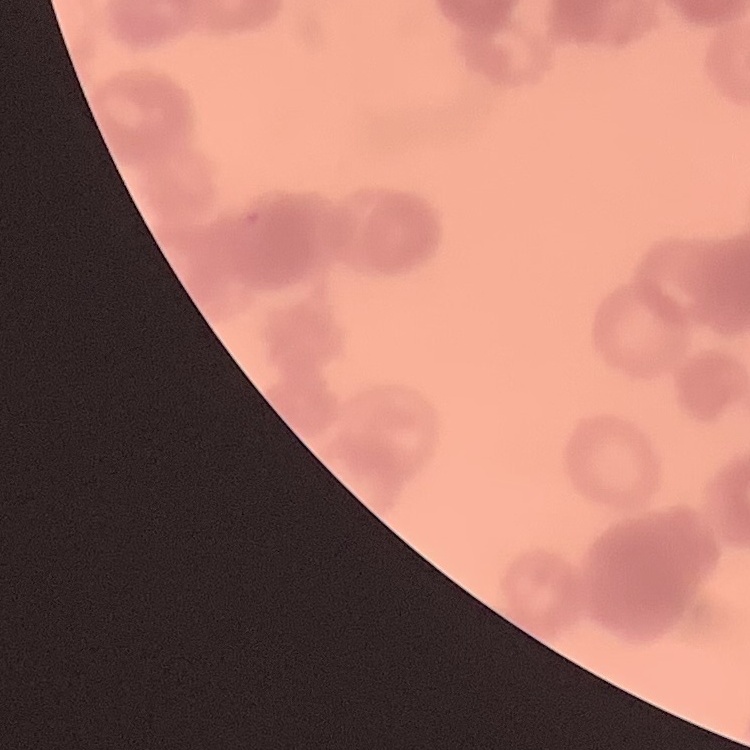
Summary:
  - Red blood cell morphology: rouleaux formation
  - Stain: Field's or Giemsa
  - Image type: square crop of a larger photomicrograph
  - Preparation: thin peripheral smear